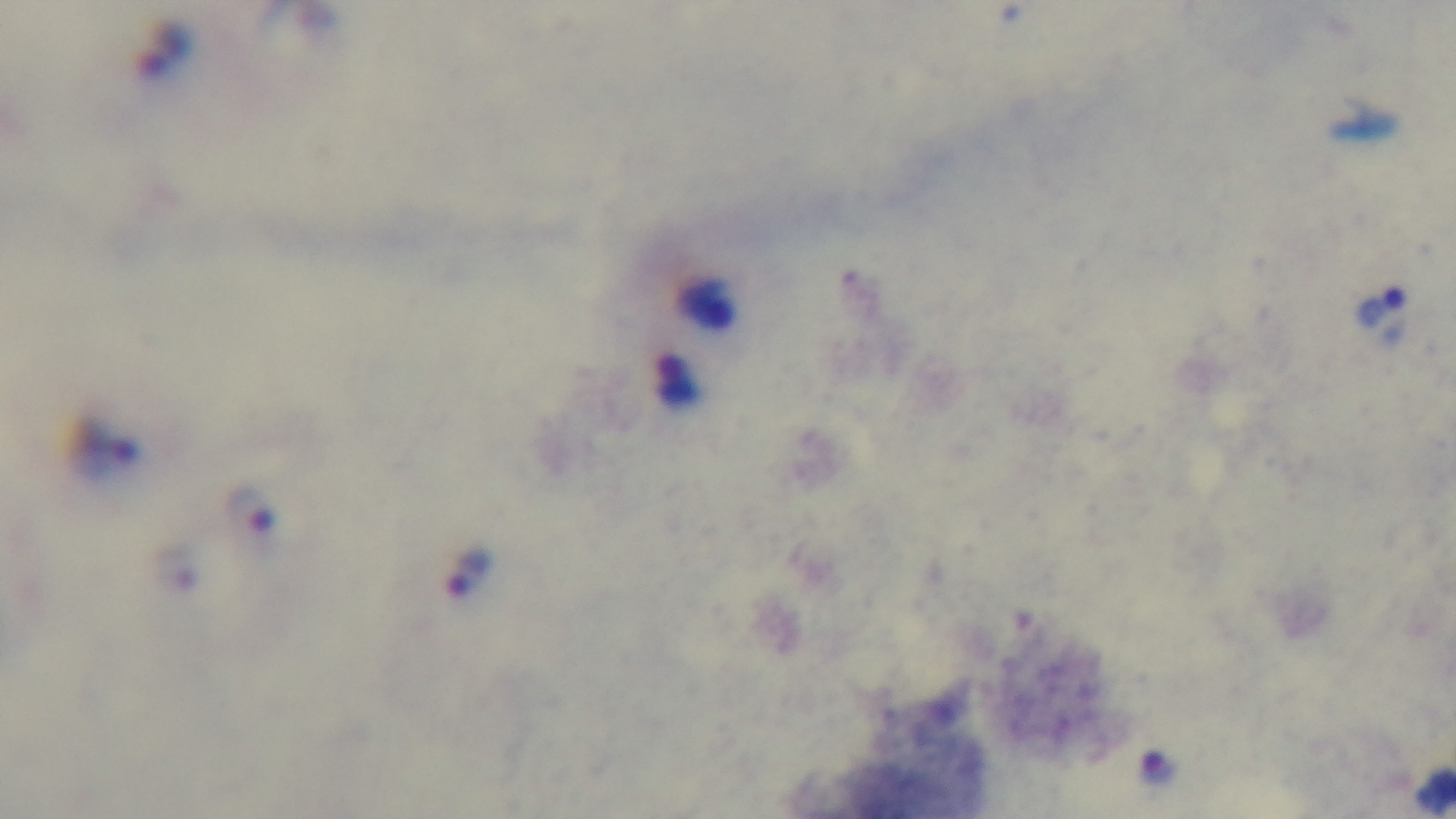

Summary:
  - Capture: mounted 4K digital camera
  - Stain: Giemsa
  - Modality: light microscopy
  - Field of view: one from the slide
  - Malaria status: infected
  - Preparation: thick
  - Objective: 100x oil immersion